Locate every blood parasite and identify its species.
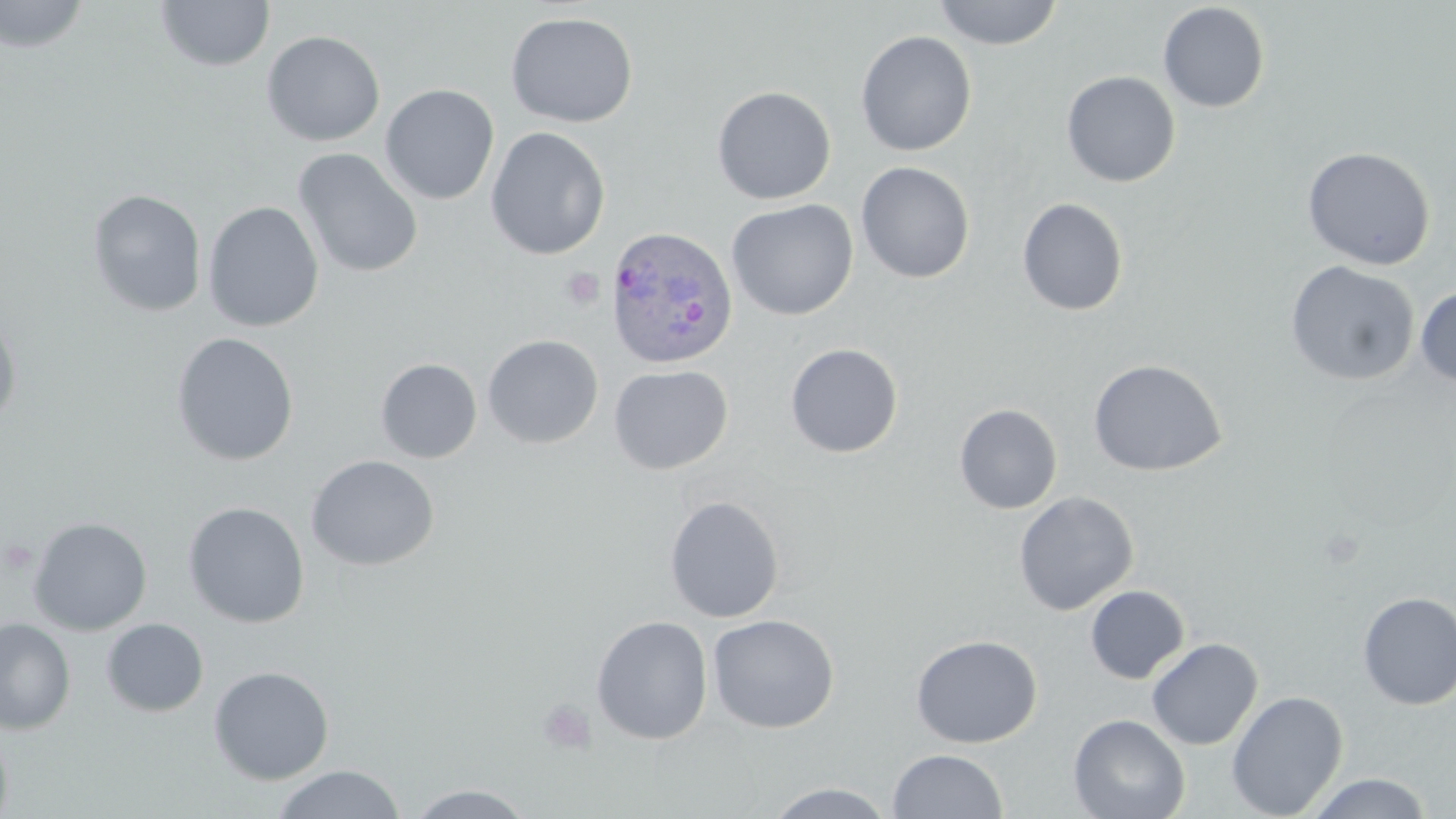

Approximate bounding boxes as (x1,y1)-(x2,y2) corner pairs in pixels.
Plasmodium ovale-infected red blood cells: (604,225)-(738,371).
No Plasmodium falciparum, Plasmodium malariae, Plasmodium vivax, Babesia divergens, or Trypanosoma brucei observed.

slide_level_diagnosis: Plasmodium ovale
field_of_view: single
stain: May-Grünwald-Giemsa
modality: optical microscopy
platelet_locations: 'approximate bounding boxes as (x1,y1)-(x2,y2) corner pairs in pixels: (561,267)-(604,310), (536,697)-(598,756)'
magnification: 1000x
preparation: thin blood smear
uninfected_red_blood_cell_locations: 'approximate bounding boxes as (x1,y1)-(x2,y2) corner pairs in pixels: (0,0)-(91,53), (932,0)-(1063,50), (155,1)-(275,72), (1158,2)-(1270,113), (505,11)-(638,128), (262,30)-(386,146), (855,30)-(977,157), (1061,70)-(1181,187), (380,84)-(500,205), (711,85)-(836,205), (485,127)-(611,260), (1302,146)-(1435,270), (292,147)-(423,278), (856,161)-(975,284), (87,189)-(207,317), (1016,197)-(1129,316), (726,199)-(858,320), (203,201)-(324,332), (1284,260)-(1420,386), (1415,286)-(1456,386), (0,311)-(22,428), (170,332)-(299,466), (482,334)-(603,449), (785,343)-(903,457), (375,358)-(482,463), (1088,359)-(1228,477), (608,364)-(733,475), (954,404)-(1062,514), (306,454)-(439,571), (1013,491)-(1139,615), (664,495)-(784,623), (183,501)-(310,628), (28,516)-(152,635), (1085,585)-(1189,684), (1357,591)-(1456,711), (707,614)-(839,734), (591,615)-(712,744), (0,617)-(76,735), (101,618)-(209,718), (911,634)-(1043,748), (1146,637)-(1263,750), (209,665)-(334,785), (1226,690)-(1348,818), (1068,713)-(1190,819), (0,726)-(13,819), (887,749)-(1008,818), (272,765)-(405,819), (1305,772)-(1433,818), (764,781)-(897,818), (405,784)-(538,818)'
image_size: 1456×819 pixels